Report the malaria status of this cell.
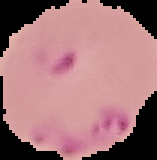

It is parasitized.

Summary:
  - Preparation: thin blood smear
  - Image type: cell region segmented out of the field of view; surrounding area masked to black
  - Image size: 157×160 pixels